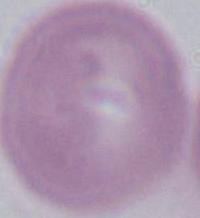

Summary:
  - Magnification: 1000x
  - Identification: erythrocyte
  - Modality: micrograph